Name the cell type shown.
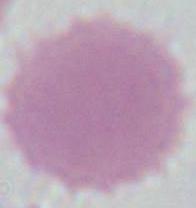

This is an erythrocyte.

modality = micrograph
magnification = 1000x